Report the malaria status of this cell.
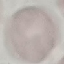
Uninfected.

Summary:
  - Image type: cell patch, automatically extracted from a larger field of view and resized to 64 × 64 pixels
  - Capture: smartphone through the microscope eyepiece
  - Preparation: thin blood smear
  - Stain: Giemsa